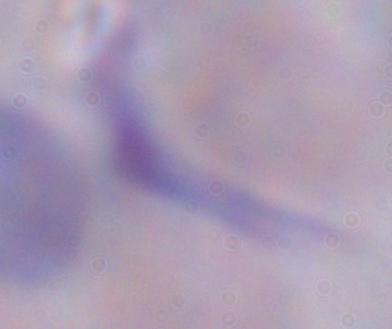
Summary:
  - Modality: micrograph
  - Magnification: 1000x
  - Identification: trypanosome